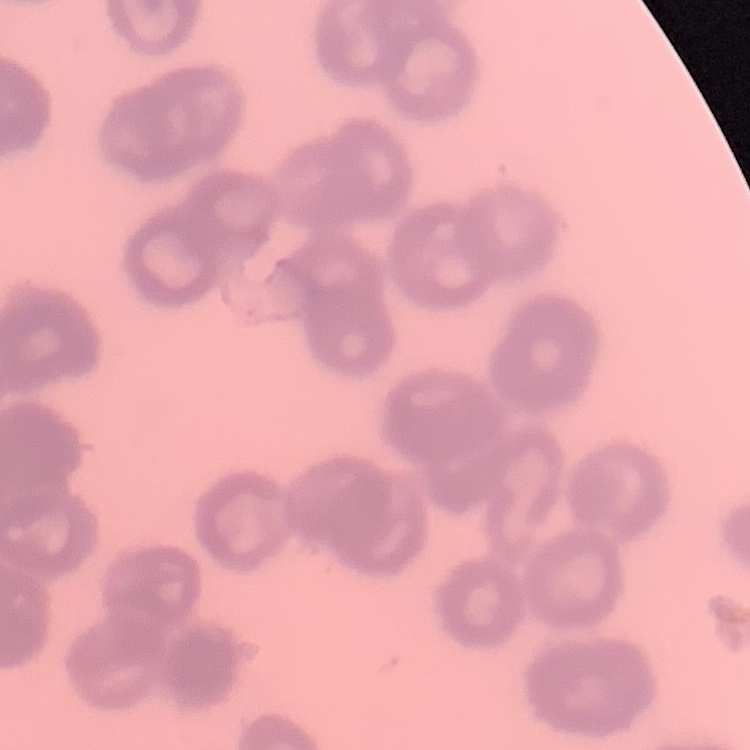

{
  "erythrocyte_morphology": "rouleaux formation",
  "image_type": "square crop of a larger photomicrograph",
  "preparation": "thin blood smear",
  "stain": "Field's or Giemsa"
}